Identify the parasite.
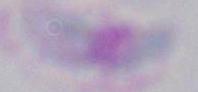
This is Toxoplasma gondii.

magnification = 1000x
modality = photomicrograph